State which parasite is depicted.
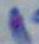

Toxoplasma gondii.

Summary:
  - Magnification: 1000x
  - Modality: micrograph